Identify the preparation type.
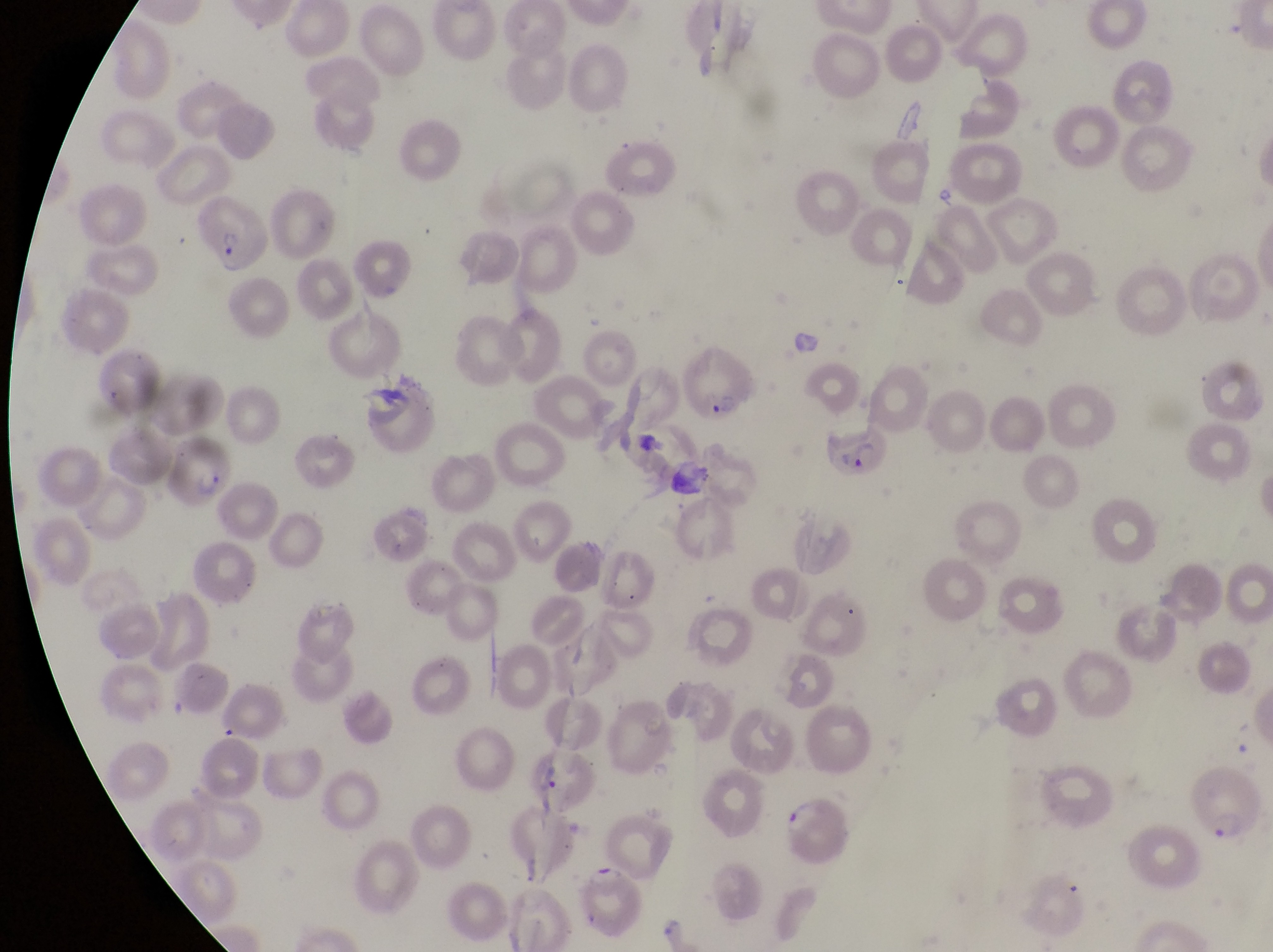

Thin blood smear.

Approximate bounding boxes as (left, top, right, bottom) in pixels.
Summary:
  - Parasitised red blood cell locations: (192, 195, 274, 273), (682, 350, 760, 427), (822, 430, 894, 485), (177, 439, 235, 509), (526, 751, 593, 819), (1188, 766, 1265, 848), (781, 794, 853, 871), (579, 861, 648, 942)
  - Field of view: single
  - Magnification: 1000x
  - Image size: 1273×952 pixels
  - Country: Uganda
  - Capture: smartphone photograph through the eyepiece of an Olympus CX-23 microscope